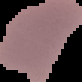
malaria status = uninfected
image type = segmented cell region on a black background
preparation = thin blood film
image size = 82×82 pixels